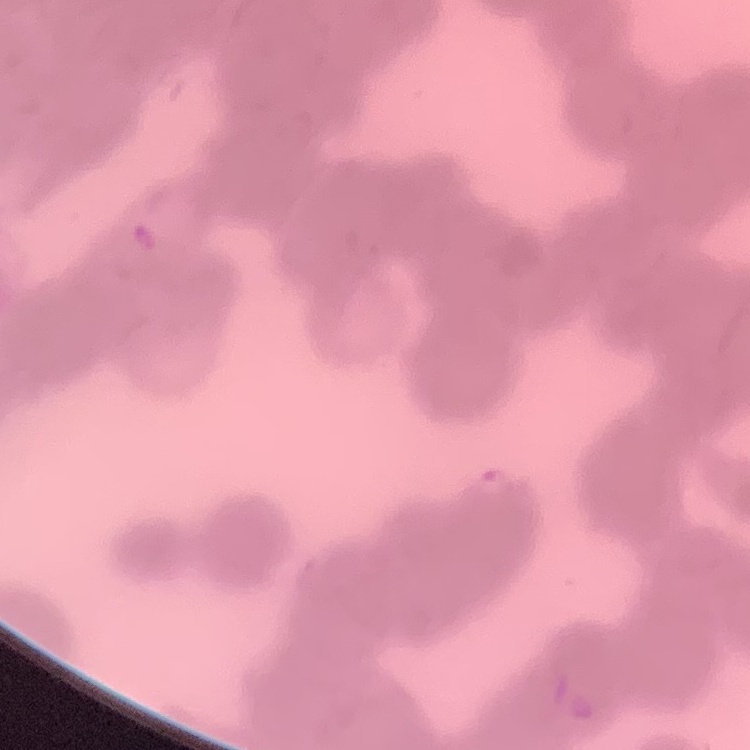 The red blood cells show rouleaux formation. One tile cut from a larger photomicrograph. Stained with either Field's or Giemsa. Thin peripheral smear.